Assess the morphology of the red blood cells.
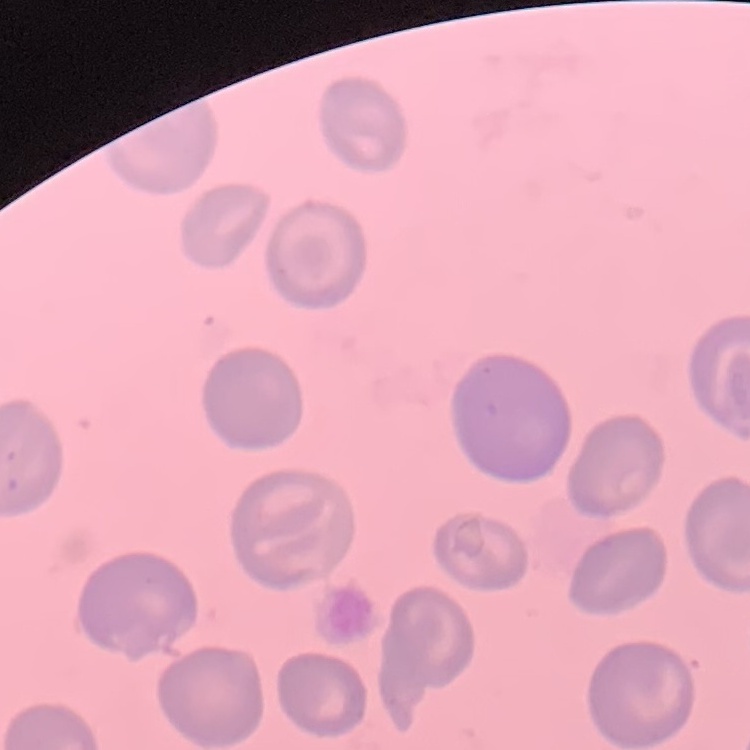
No rouleaux formation.

Summary:
  - Image type: one tile cut from a larger photomicrograph
  - Preparation: thin peripheral smear
  - Stain: Field's or Giemsa